Assess the morphology of the red blood cells.
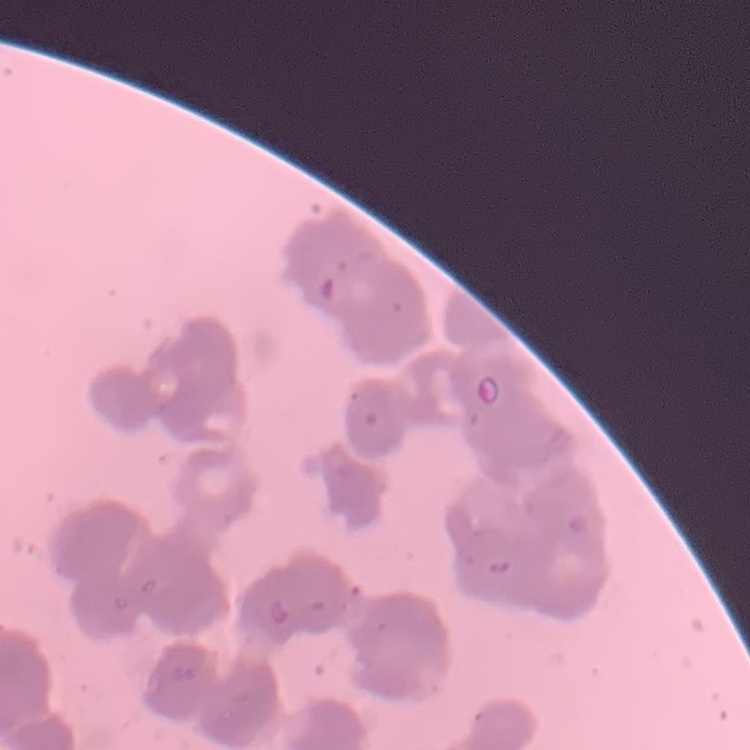

Rouleaux formation.

stain: Field's or Giemsa
preparation: thin blood film
image_type: square crop of a larger photomicrograph